Report the malaria status of this cell.
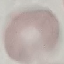

It is uninfected.

{
  "capture": "smartphone camera at the microscope eyepiece",
  "stain": "Giemsa",
  "image_type": "automatically extracted cell patch, resized to 64 × 64 pixels",
  "preparation": "thin smear"
}